Assess this cell for malaria.
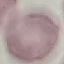
Uninfected.

Thin smear of blood. Acquired by smartphone through the microscope eyepiece. Automatically extracted cell patch, resized to 64 × 64 pixels. Giemsa stain.